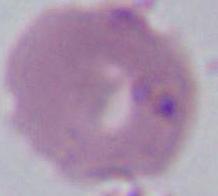

identification = erythrocyte
modality = photomicrograph
magnification = 1000x